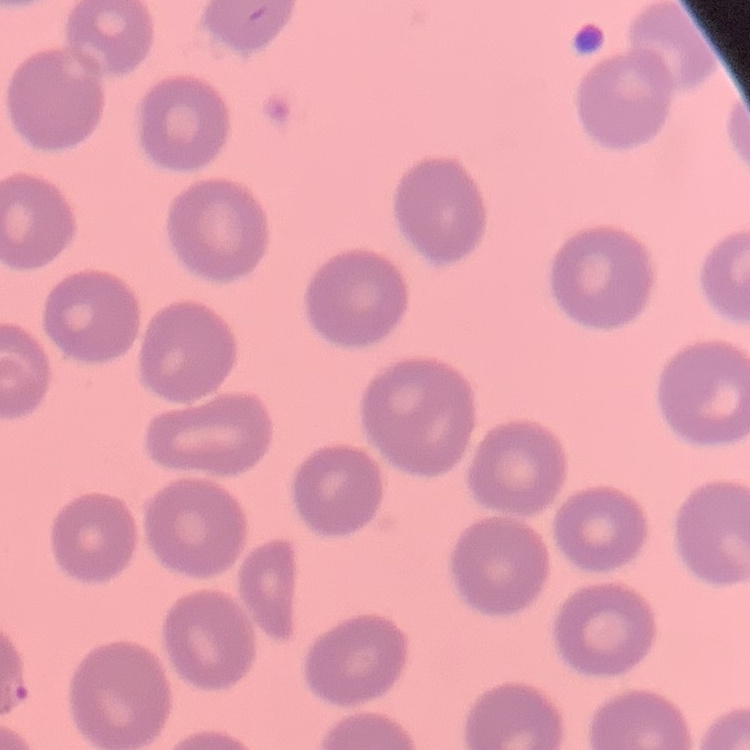
The erythrocytes exhibit no rouleaux formation. Thin blood smear. Field's or Giemsa stain. One tile cut from a larger photomicrograph.